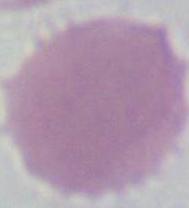 Captured at 1000x magnification. Micrograph. An erythrocyte is seen.